Identify the cell.
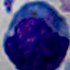
This is a leukocyte.

modality = photomicrograph
magnification = 1000x